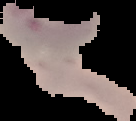
Summary:
  - Preparation: thin blood film
  - Image type: cell region segmented out of the field of view; surrounding area masked to black
  - Result: Plasmodium parasites detected
  - Image size: 136×121 pixels